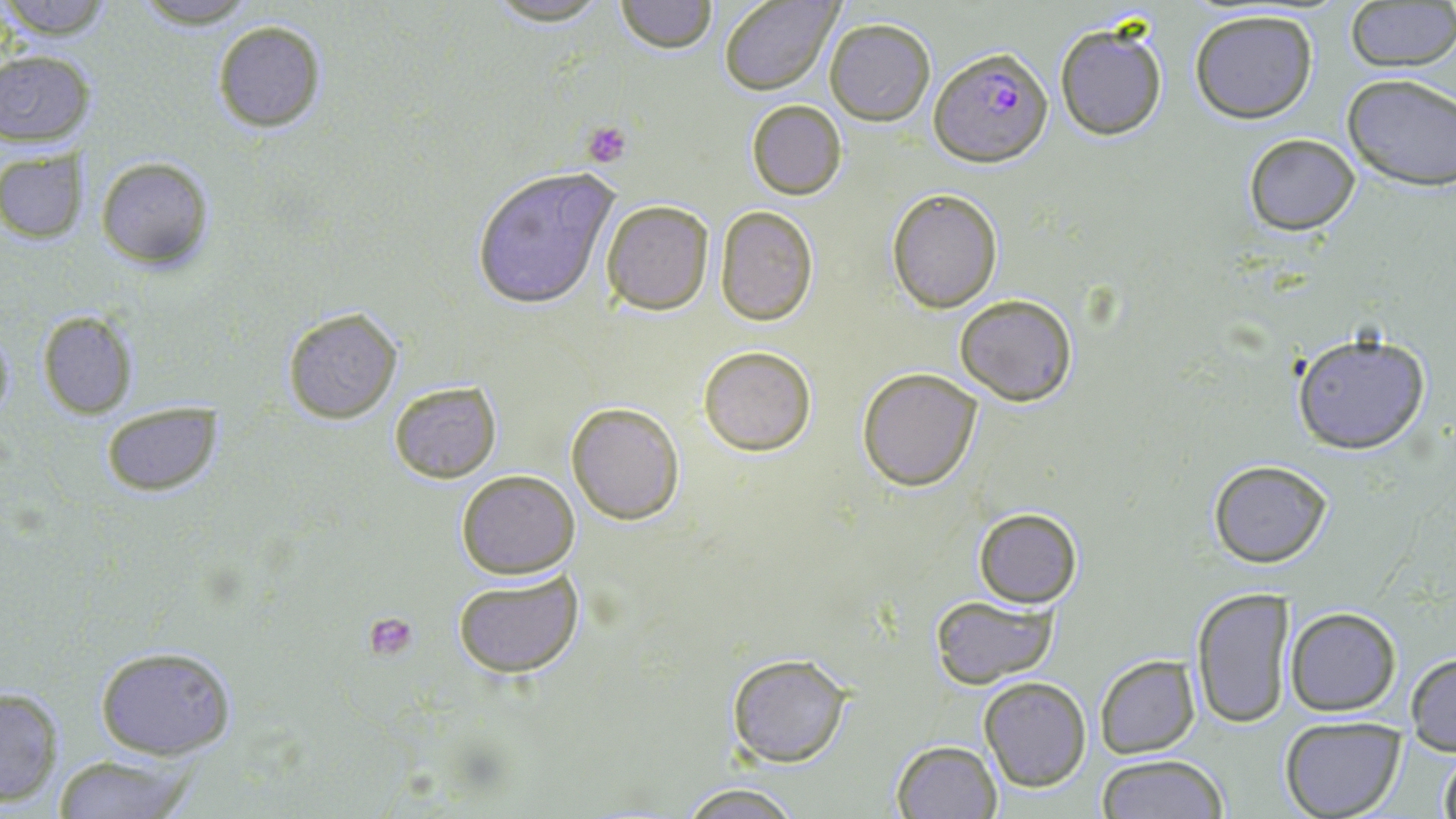
Approximate bounding boxes as (x1, y1, x2, y2) in pixels. Uninfected red blood cell locations: (0, 0, 119, 40), (127, 0, 265, 29), (481, 0, 615, 26), (614, 0, 717, 53), (717, 0, 841, 94), (1344, 1, 1454, 71), (1189, 8, 1320, 123), (825, 17, 936, 125), (211, 20, 327, 132), (1054, 21, 1169, 141), (0, 50, 93, 146), (1341, 72, 1456, 192), (746, 100, 846, 200), (1241, 133, 1361, 236), (0, 147, 83, 243), (94, 156, 215, 270), (470, 165, 623, 309), (887, 187, 1002, 312), (601, 201, 716, 315), (714, 206, 819, 324), (953, 293, 1078, 407), (283, 307, 402, 423), (37, 311, 137, 418), (0, 327, 15, 423), (1290, 329, 1433, 455), (698, 345, 816, 457), (857, 366, 982, 492), (388, 381, 502, 482), (567, 400, 685, 523), (102, 402, 221, 495), (1207, 459, 1332, 568), (455, 468, 581, 579), (973, 507, 1084, 607), (452, 568, 586, 680), (1189, 586, 1296, 728), (931, 596, 1059, 686), (1285, 607, 1400, 715), (93, 643, 237, 759), (725, 651, 853, 769), (1405, 652, 1455, 753), (1094, 655, 1200, 757), (978, 677, 1091, 792), (0, 685, 64, 807), (1277, 716, 1406, 819), (891, 739, 1001, 819), (1437, 747, 1456, 819), (50, 752, 205, 817), (1094, 754, 1227, 819), (673, 782, 813, 818). Platelet locations: (582, 121, 633, 166), (364, 614, 419, 658). Plasmodium falciparum-infected red blood cell locations: (930, 48, 1053, 166). Slide-level diagnosis: Plasmodium falciparum. Thin blood film. Image is 1456×819 pixels. Optical microscopy. May-Grünwald-Giemsa stain. 1000x magnification. One field of a larger specimen.